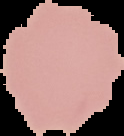

preparation: thin blood film
image_type: segmented cell region with the area outside set to black
image_size: 124×136 pixels
malaria_status: uninfected